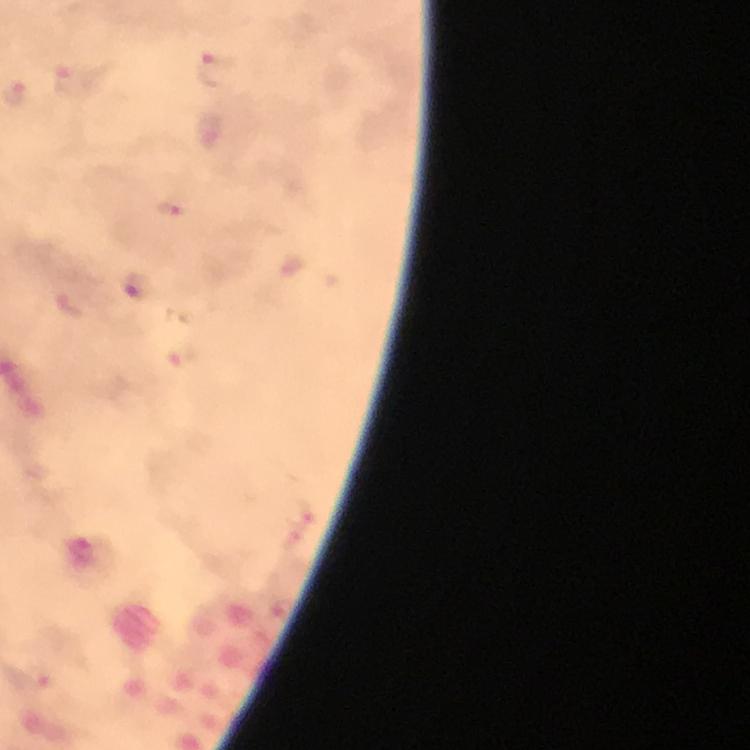
Approximate centers as [x, y] in pixels. Malaria parasite locations: [215, 70], [78, 83], [170, 209], [137, 287]. 100x magnification. Immersion oil was used. Thick smear. Cropped region of a single field of view. From a diagnostic examination for malaria. Image is 750×750 pixels. Giemsa-stained preparation. Photographed with a smartphone mounted on the microscope.